Classify this cell by malaria status.
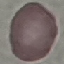

It is uninfected.

Summary:
  - Capture: smartphone camera at the microscope eyepiece
  - Image type: cell patch, automatically extracted from a larger field of view and resized to 64 × 64 pixels
  - Preparation: thin blood smear
  - Stain: Giemsa